Report the malaria status of this cell.
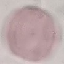
Uninfected.

Thin blood smear. Giemsa-stained preparation. Automatically extracted cell patch, resized to 64 × 64 pixels. Photographed with a smartphone camera at the microscope eyepiece.